Identify the preparation type.
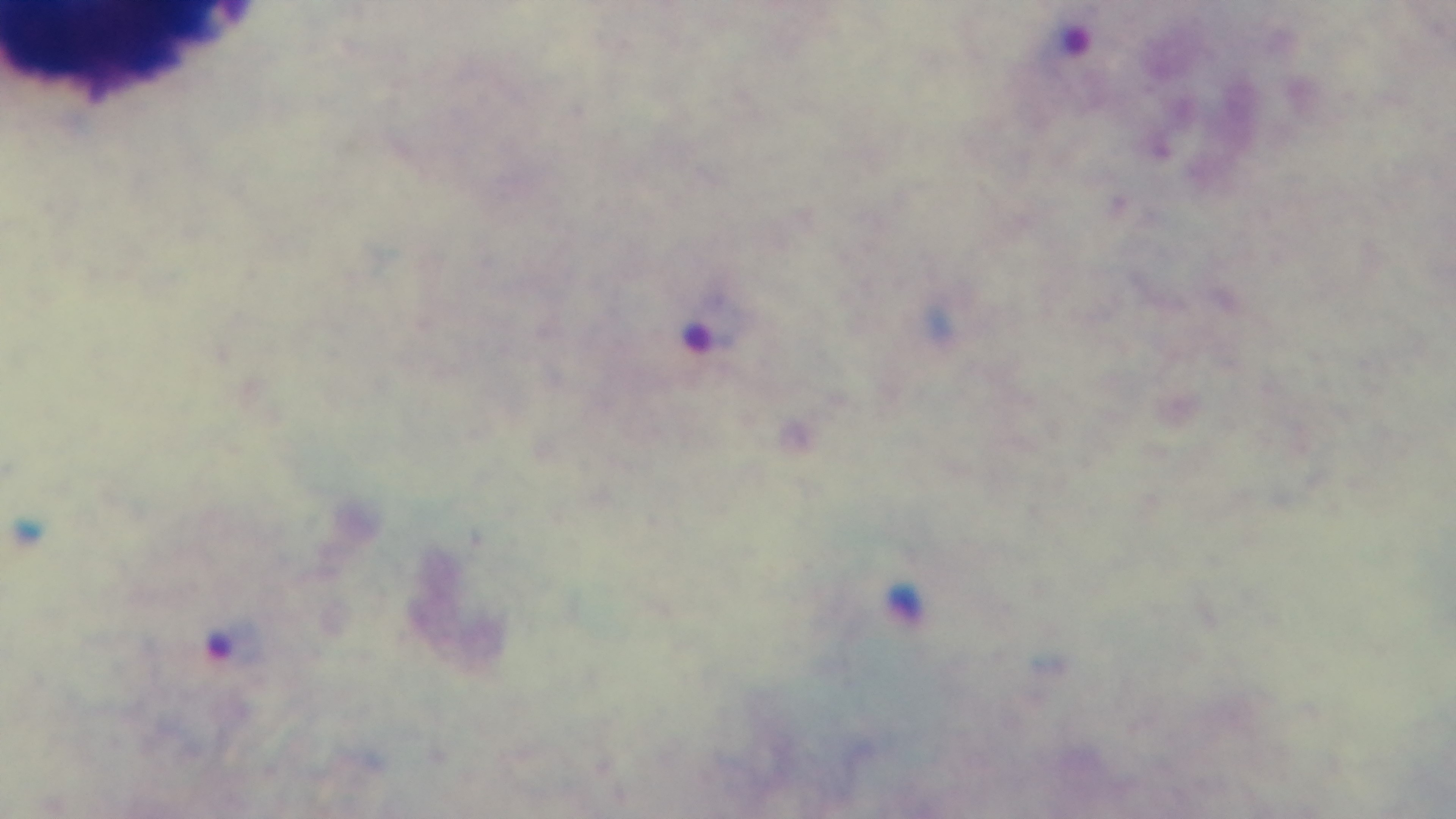
A thick smear.

field of view = one from the slide
modality = light microscopy
objective = 100x oil immersion
stain = Giemsa
capture = mounted 4K digital camera
malaria status = positive